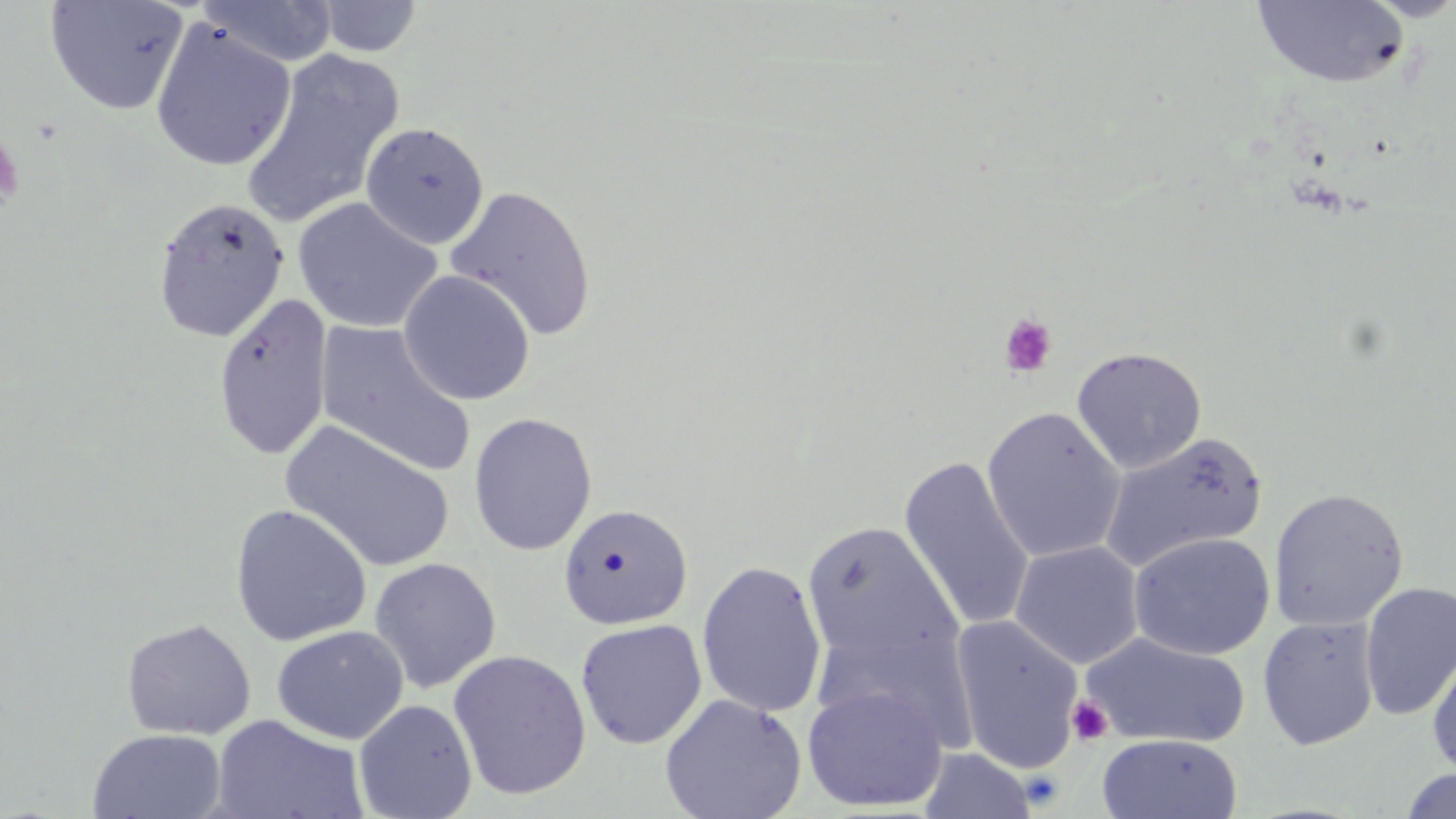
Approximate bounding boxes as [x1, y1, x2, y2] in pixels. Uninfected red blood cell locations: [44, 0, 190, 115], [198, 0, 339, 68], [314, 0, 423, 58], [1362, 0, 1456, 22], [1250, 1, 1412, 89], [150, 20, 296, 171], [241, 50, 404, 227], [361, 122, 489, 249], [444, 185, 598, 342], [151, 197, 290, 342], [292, 197, 443, 334], [398, 270, 536, 406], [212, 294, 333, 461], [316, 322, 477, 478], [1071, 346, 1207, 474], [981, 406, 1127, 563], [468, 412, 597, 556], [281, 420, 456, 573], [1099, 431, 1269, 572], [898, 455, 1036, 634], [1269, 487, 1409, 632], [558, 503, 693, 630], [230, 504, 372, 646], [801, 520, 963, 669], [1128, 532, 1276, 660], [1009, 541, 1144, 668], [368, 557, 502, 693], [696, 560, 827, 718], [1359, 581, 1456, 721], [950, 615, 1086, 773], [1257, 616, 1380, 750], [121, 618, 256, 739], [575, 618, 707, 749], [812, 622, 983, 755], [272, 625, 409, 744], [1081, 631, 1251, 749], [1427, 645, 1456, 777], [447, 649, 592, 801], [801, 683, 950, 812], [659, 694, 807, 819], [354, 699, 478, 819], [211, 715, 369, 819], [87, 728, 227, 818], [1097, 734, 1242, 818], [917, 746, 1038, 819], [1397, 769, 1456, 819]. Platelet locations: [0, 130, 25, 215], [999, 313, 1058, 378], [1068, 694, 1113, 746]. Slide-level diagnosis: negative for blood parasites. May-Grünwald-Giemsa-stained preparation. Single field of view. Thin blood smear. Image is 1456×819 pixels. Light microscopy. Captured at 1000x magnification.